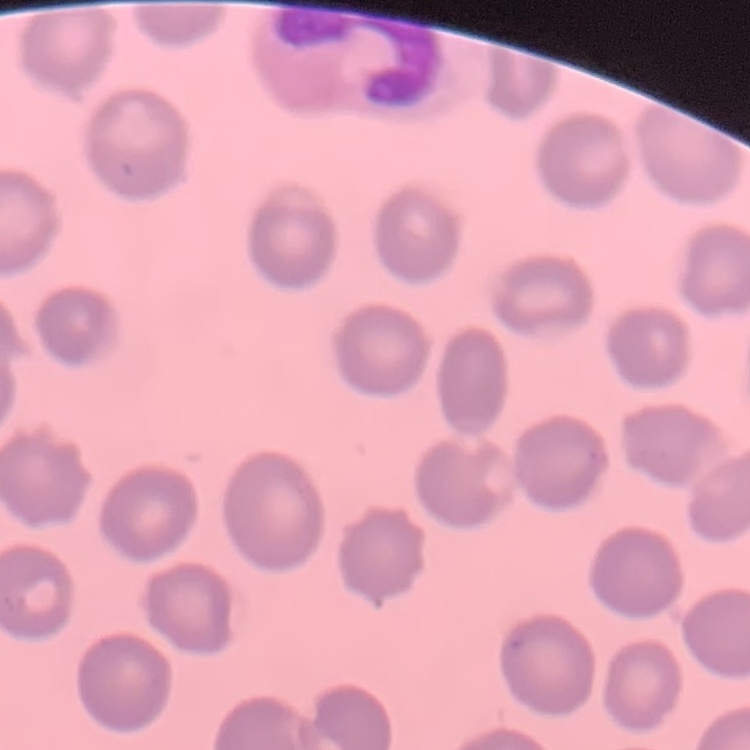
The red blood cells exhibit no rouleaux formation. Square crop of a larger photomicrograph. Thin peripheral smear. Stained with either Field's or Giemsa.